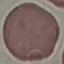

Malaria status: uninfected. Giemsa stain. Cell patch, automatically extracted from a larger field of view and resized to 64 × 64 pixels. Thin smear of blood. Acquired by smartphone through the microscope eyepiece.